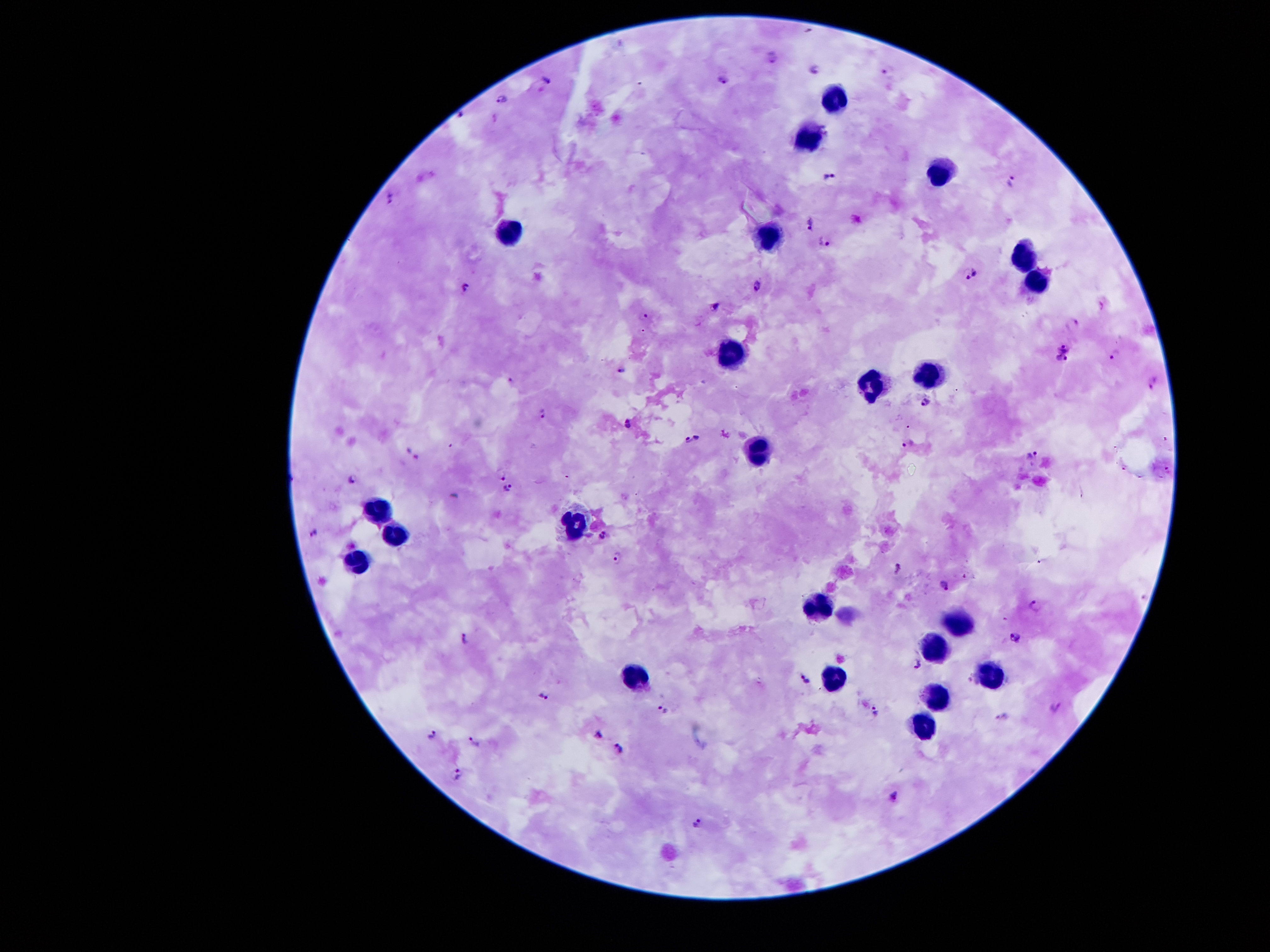
coordinate format = approximate object centers, in pixels from the top-left corner
leukocyte locations = (x=835, y=97), (x=807, y=139), (x=935, y=167), (x=515, y=230), (x=769, y=234), (x=1023, y=253), (x=1034, y=284), (x=734, y=355), (x=930, y=370), (x=871, y=382), (x=758, y=449), (x=375, y=507), (x=578, y=520), (x=400, y=534), (x=359, y=559), (x=821, y=607), (x=959, y=625), (x=935, y=643), (x=990, y=675), (x=836, y=678), (x=637, y=679), (x=939, y=695), (x=927, y=721)
malaria parasite locations = (x=772, y=58), (x=815, y=68), (x=887, y=70), (x=724, y=79), (x=545, y=85), (x=501, y=98), (x=828, y=177), (x=1010, y=180), (x=390, y=196), (x=810, y=222), (x=825, y=242), (x=970, y=276), (x=464, y=286), (x=756, y=286), (x=717, y=306), (x=643, y=315), (x=1073, y=323), (x=1064, y=348), (x=1115, y=354), (x=1061, y=360), (x=622, y=369), (x=510, y=379), (x=1153, y=380), (x=925, y=400), (x=544, y=412), (x=628, y=422), (x=697, y=437), (x=688, y=440), (x=907, y=442), (x=1033, y=455), (x=501, y=474), (x=353, y=478), (x=507, y=487), (x=315, y=534), (x=603, y=534), (x=616, y=557), (x=897, y=566), (x=943, y=584), (x=1034, y=606), (x=1014, y=635), (x=466, y=639), (x=917, y=664), (x=805, y=679), (x=546, y=696), (x=663, y=709), (x=1054, y=709), (x=876, y=712), (x=1002, y=715), (x=597, y=735), (x=432, y=736), (x=475, y=740), (x=620, y=748), (x=458, y=772), (x=895, y=796), (x=696, y=822)
magnification = 100x
field of view = one from this slide
preparation = thick blood film
capture = smartphone through the microscope eyepiece
image size = 1270×952 pixels
stain = Giemsa
patient malaria status = infected with Plasmodium falciparum